State the preparation type.
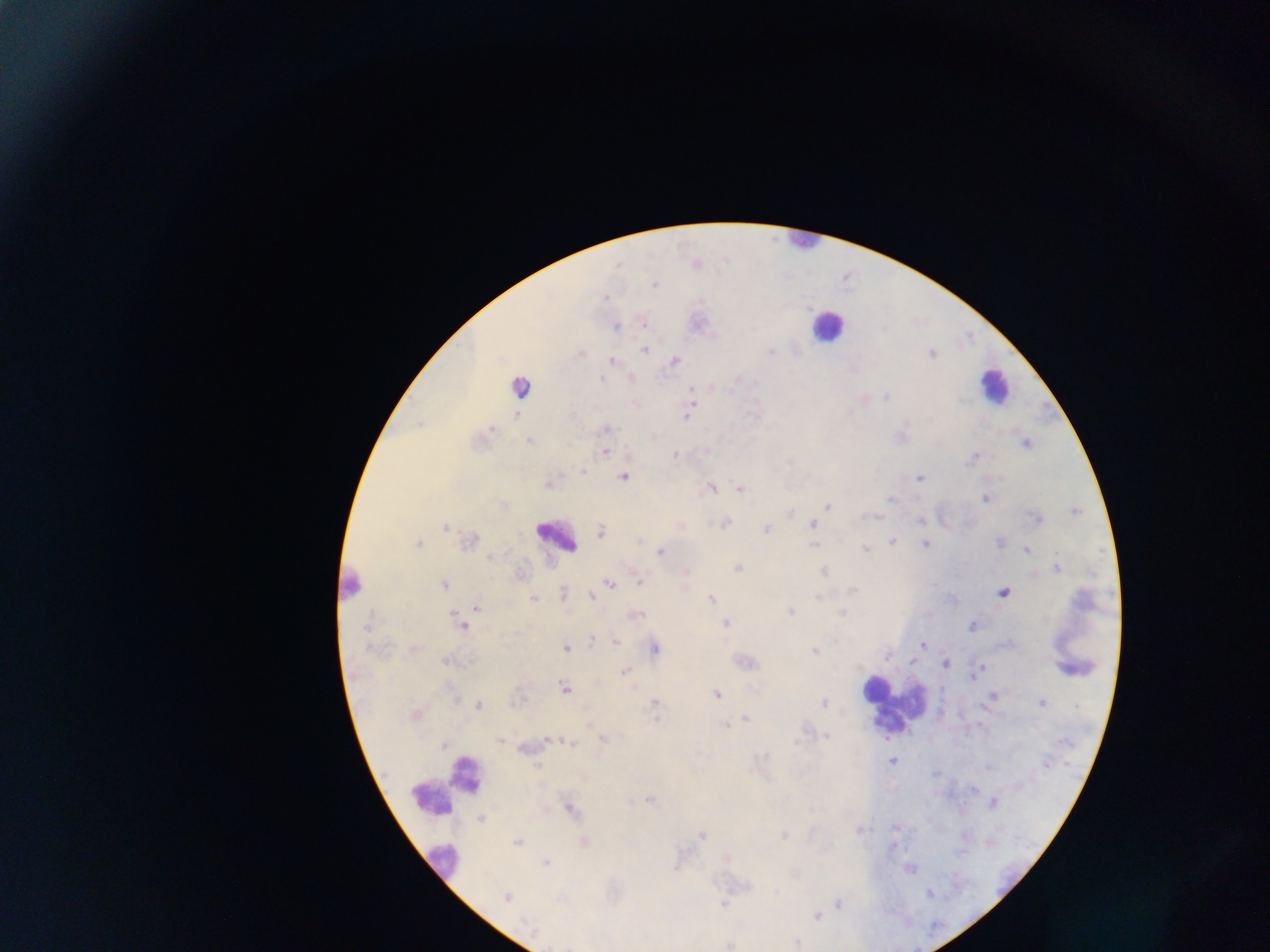
This is a thick smear.

{
  "plasmodium_parasite_locations": "approximate centers as [x, y] in pixels: [696, 264], [654, 283], [605, 297], [643, 321], [615, 327], [645, 349], [770, 352], [580, 353], [931, 353], [613, 361], [674, 361], [631, 378], [710, 385], [886, 395], [688, 414], [516, 415], [605, 429], [529, 440], [1026, 444], [604, 452], [676, 455], [975, 456], [582, 471], [623, 477], [920, 478], [549, 484], [710, 488], [740, 489], [985, 498], [827, 505], [1075, 511], [1036, 518], [921, 519], [943, 520], [724, 523], [812, 524], [446, 526], [678, 526], [765, 529], [601, 532], [469, 541], [893, 541], [926, 543], [999, 543], [417, 544], [815, 544], [865, 550], [1027, 550], [661, 551], [489, 557], [738, 567], [1057, 567], [823, 571], [519, 575], [639, 580], [609, 584], [444, 585], [852, 590], [1003, 592], [563, 593], [590, 597], [533, 598], [711, 598], [475, 605], [789, 611], [842, 612], [633, 614], [461, 623], [726, 623], [972, 625], [367, 627], [591, 640], [615, 641], [923, 645], [565, 647], [413, 648], [653, 648], [814, 650], [446, 661], [911, 662], [945, 663], [625, 671], [977, 671], [564, 688], [716, 694], [993, 698], [653, 702], [1043, 702], [823, 703], [477, 704], [415, 714], [745, 718], [590, 725], [725, 725], [827, 736], [499, 739], [602, 739], [546, 741], [570, 742], [526, 747], [892, 761], [649, 799], [992, 802], [568, 808], [480, 819], [896, 827], [859, 830], [701, 835], [783, 836], [517, 842], [584, 842], [892, 846], [545, 862], [677, 864], [908, 868], [507, 897], [838, 903], [724, 904], [816, 915], [796, 942], [731, 943]",
  "leukocyte_locations": "approximate centers as [x, y] in pixels: [802, 240], [827, 326], [522, 385], [995, 387], [556, 536], [352, 585], [1076, 667], [893, 705], [467, 777], [447, 786], [442, 860]",
  "capture": "mobile-phone photograph through a microscope",
  "field_of_view": "single",
  "image_size": "1270×952 pixels",
  "country": "Ghana"
}